Assess this cell for malaria.
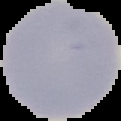

Uninfected.

image_type: cell region segmented out of the field of view; surrounding area masked to black
preparation: thin blood film
image_size: 121×121 pixels